Report the malaria status of this cell.
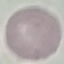
Uninfected.

Thin blood film. Photographed with a smartphone camera at the microscope eyepiece. Giemsa stain. Automatically extracted cell patch, resized to 64 × 64 pixels.